Classify this cell by malaria status.
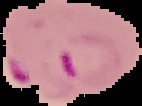
It is parasitized.

Summary:
  - Preparation: thin blood smear
  - Image type: segmented cell region with the area outside set to black
  - Image size: 142×106 pixels